Locate and identify every blood parasite.
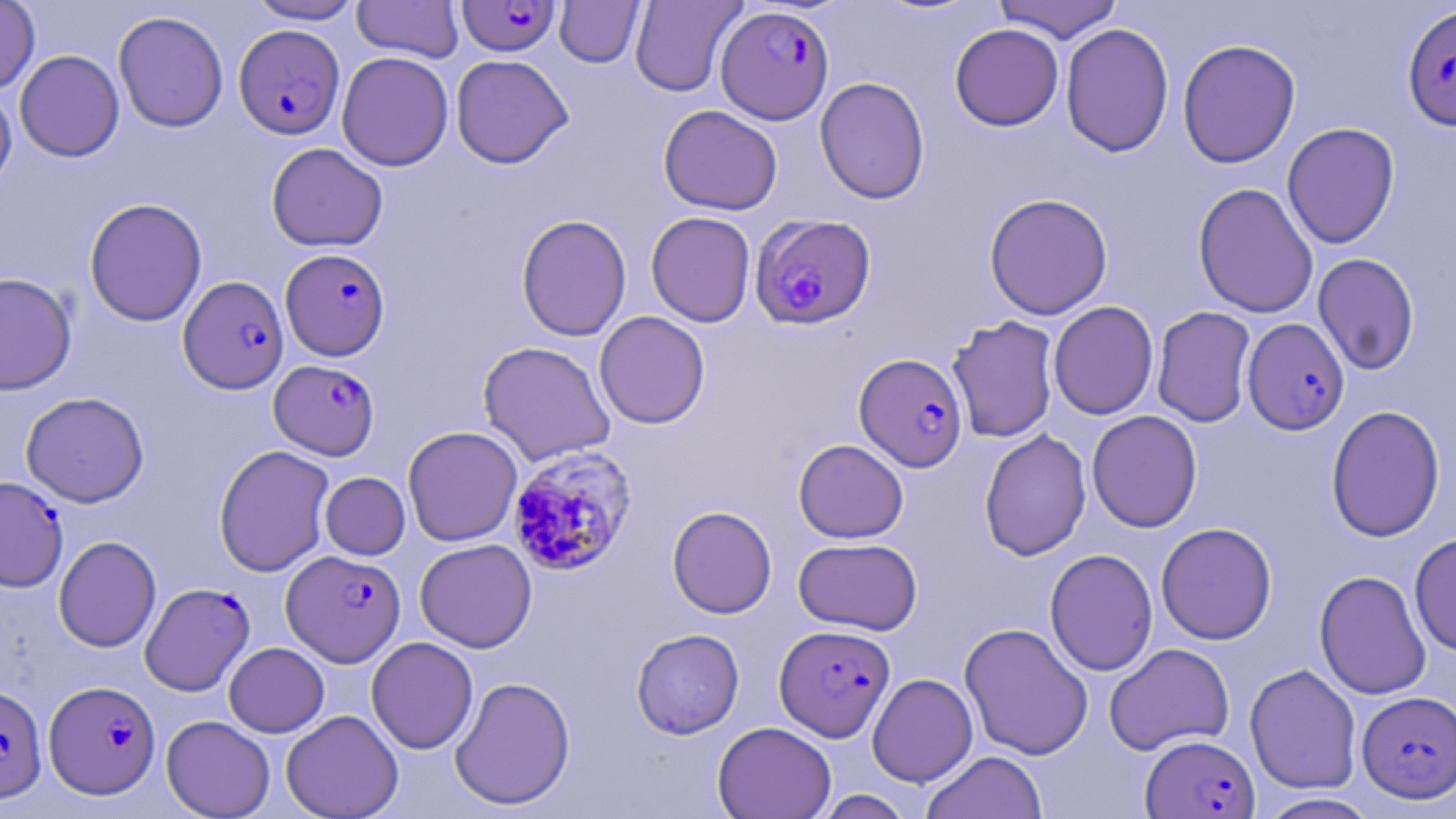
Approximate bounding boxes as [x1, y1, x2, y2] in pixels.
Plasmodium falciparum-infected red blood cells: [457, 0, 561, 57], [1402, 4, 1456, 132], [716, 5, 835, 124], [234, 24, 345, 139], [749, 213, 877, 330], [280, 248, 390, 361], [178, 275, 289, 393], [1242, 317, 1349, 434], [854, 353, 968, 472], [269, 359, 380, 460], [508, 450, 640, 582], [0, 476, 69, 592], [282, 549, 405, 666], [140, 583, 254, 695], [774, 624, 895, 742], [45, 680, 160, 798], [0, 683, 47, 804], [1357, 691, 1456, 802], [1141, 734, 1258, 818].
No Plasmodium ovale, Plasmodium malariae, Plasmodium vivax, Babesia divergens, or Trypanosoma brucei observed.

Uninfected red blood cell locations: [246, 0, 365, 25], [352, 0, 464, 63], [992, 0, 1124, 43], [0, 1, 40, 95], [554, 1, 645, 67], [630, 1, 745, 97], [113, 10, 229, 133], [1060, 23, 1175, 158], [949, 24, 1064, 131], [1177, 39, 1300, 168], [14, 49, 125, 162], [336, 51, 454, 171], [450, 54, 574, 168], [814, 76, 930, 205], [0, 84, 17, 196], [658, 104, 783, 215], [1282, 122, 1400, 249], [266, 142, 388, 251], [1193, 183, 1319, 318], [984, 192, 1113, 320], [84, 198, 207, 326], [645, 211, 756, 327], [516, 214, 632, 341], [1312, 253, 1420, 375], [0, 272, 77, 395], [1048, 301, 1158, 420], [1151, 306, 1257, 428], [594, 311, 711, 429], [947, 315, 1060, 443], [478, 341, 616, 466], [21, 391, 149, 508], [1325, 404, 1446, 542], [1087, 410, 1202, 533], [403, 425, 523, 546], [979, 429, 1091, 561], [793, 439, 909, 543], [213, 444, 335, 577], [320, 472, 410, 560], [667, 505, 777, 619], [1155, 522, 1277, 645], [1409, 533, 1456, 656], [54, 535, 162, 652], [793, 537, 922, 635], [415, 538, 537, 653], [1044, 548, 1158, 676], [1314, 570, 1431, 700], [959, 622, 1094, 760], [631, 628, 744, 739], [366, 636, 478, 754], [224, 642, 329, 737], [1104, 642, 1235, 756], [1244, 663, 1362, 795], [867, 673, 978, 787], [450, 676, 576, 810], [281, 709, 403, 819], [161, 715, 275, 818], [712, 721, 836, 819], [922, 750, 1047, 819], [813, 790, 915, 819], [1254, 793, 1383, 818]. Slide-level diagnosis: Plasmodium falciparum. Optical microscopy. Image is 1456×819 pixels. May-Grünwald-Giemsa stain. 1000x magnification. Thin blood film. Single field of view.